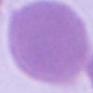 An erythrocyte is shown. 1000x magnification. Photomicrograph.